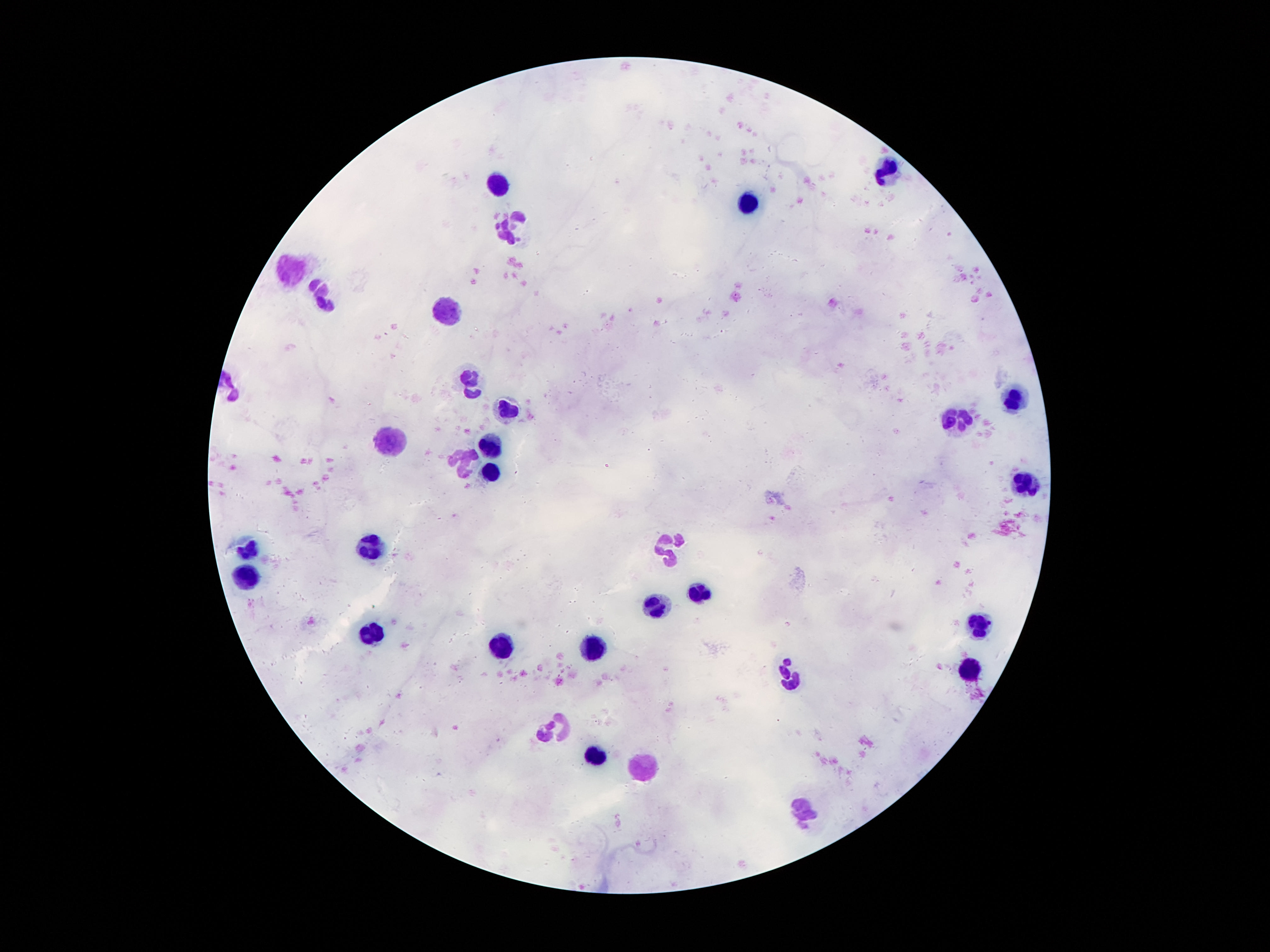 Approximate centers as (x, y) in pixels. Leukocyte locations: (885, 169), (501, 187), (749, 203), (508, 230), (291, 267), (322, 292), (445, 312), (470, 382), (1015, 398), (510, 407), (960, 419), (390, 444), (490, 446), (465, 462), (492, 469), (1026, 484), (665, 544), (248, 548), (370, 548), (245, 575), (697, 593), (654, 607), (978, 624), (374, 631), (501, 646), (595, 647), (973, 669), (790, 673), (554, 727), (597, 753), (644, 762), (806, 811). One field from this slide. Giemsa-stained preparation. Thick blood film. Photographed through the microscope eyepiece with a smartphone camera. Image is 1270×952 pixels. Patient malaria status: not infected. 100x magnification.